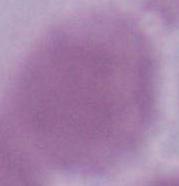 A red blood cell is seen. Micrograph. 1000x magnification.